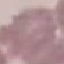 Result: no malaria parasites detected. Cell patch, automatically extracted from a larger field of view and resized to 64 × 64 pixels. Giemsa stain. Photographed with a smartphone camera at the microscope eyepiece. Thin blood smear.